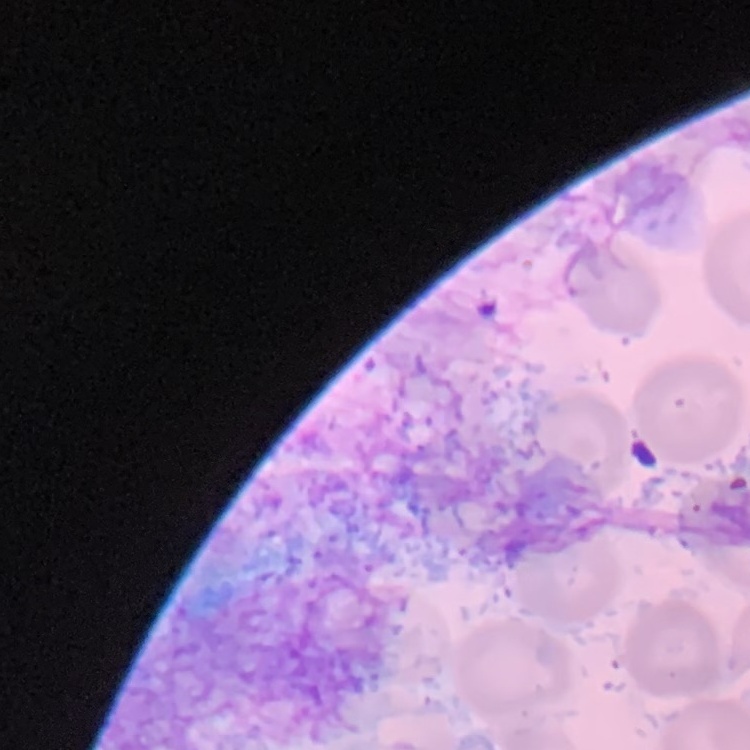
{
  "red_blood_cell_morphology": "no rouleaux formation",
  "preparation": "thin peripheral smear",
  "image_type": "square crop of a larger photomicrograph",
  "stain": "Field's or Giemsa"
}